Locate malaria parasites and leukocytes.
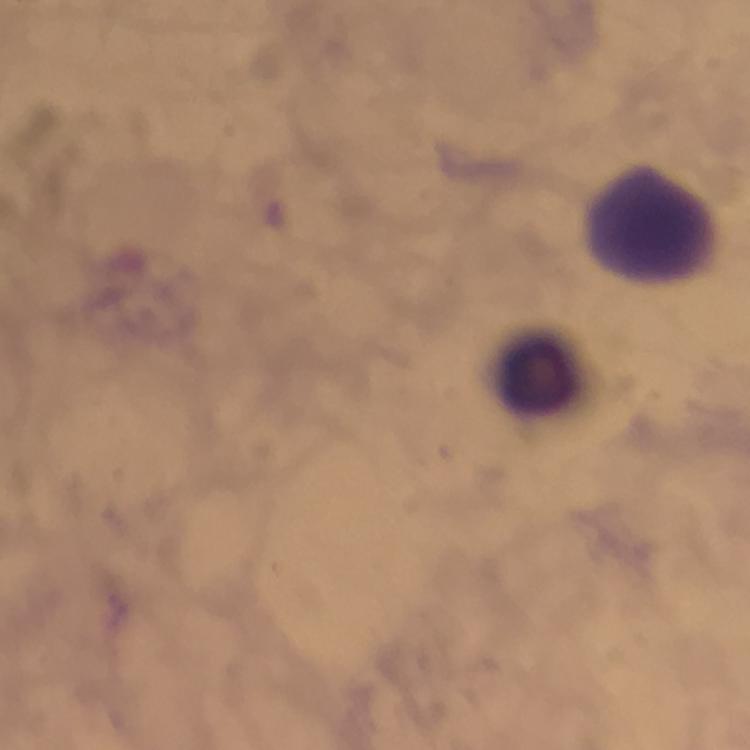

No malaria parasites seen.
Approximate centers as {x, y} in pixels.
Leukocytes: {650, 222}, {537, 366}.

Thick smear. At 100x magnification. A crop from one field of view. Giemsa stain. Photographed through the microscope with a smartphone camera. Immersion oil applied. From a diagnostic examination for malaria. Image is 750×750 pixels.